Name the blood parasite species.
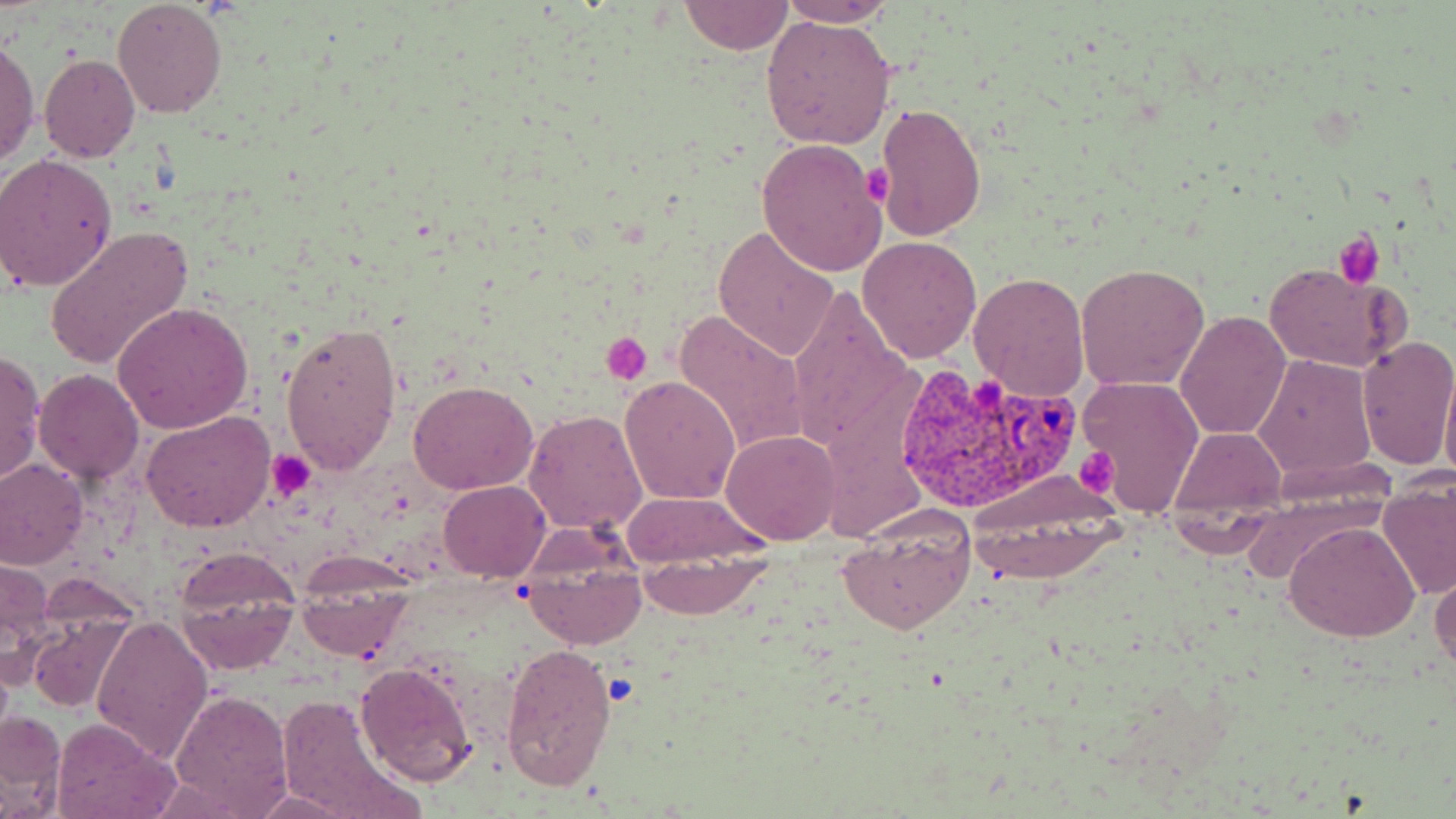

Plasmodium vivax.

{
  "image_size": "1456×819 pixels",
  "plasmodium_vivax_infected_red_blood_cell_locations": "approximate bounding boxes as [x1, y1, x2, y2] in pixels: [888, 361, 1081, 515]",
  "platelet_locations": "approximate bounding boxes as [x1, y1, x2, y2] in pixels: [864, 166, 894, 205], [1333, 230, 1385, 287], [600, 333, 652, 384], [1075, 446, 1121, 493], [269, 452, 315, 496]",
  "uninfected_red_blood_cell_locations": "approximate bounding boxes as [x1, y1, x2, y2] in pixels: [112, 1, 229, 119], [677, 1, 795, 55], [778, 1, 897, 27], [760, 16, 896, 149], [0, 37, 38, 171], [38, 54, 140, 163], [873, 102, 987, 240], [756, 139, 887, 276], [0, 153, 119, 292], [713, 225, 837, 363], [44, 226, 193, 371], [857, 236, 982, 364], [1262, 261, 1409, 373], [1075, 262, 1208, 392], [968, 270, 1090, 403], [786, 283, 914, 456], [112, 301, 254, 433], [673, 308, 807, 456], [1174, 311, 1292, 442], [280, 321, 403, 474], [1356, 335, 1456, 471], [0, 351, 46, 484], [1253, 353, 1379, 483], [1438, 362, 1456, 485], [32, 368, 144, 483], [1076, 375, 1205, 518], [619, 376, 742, 503], [408, 381, 539, 496], [525, 408, 650, 537], [141, 410, 274, 533], [1168, 426, 1286, 516], [721, 429, 840, 545], [0, 460, 86, 568], [438, 481, 550, 582], [620, 490, 770, 565], [1378, 490, 1456, 599], [961, 491, 1125, 586], [1164, 512, 1278, 557], [835, 516, 975, 636], [1284, 521, 1422, 643], [516, 528, 648, 651], [173, 547, 304, 674], [633, 552, 768, 617], [0, 554, 55, 680], [1430, 566, 1455, 679], [300, 574, 409, 660], [27, 613, 136, 715], [92, 615, 213, 763], [501, 641, 617, 791], [355, 662, 477, 787], [168, 687, 293, 819], [279, 695, 421, 818], [0, 709, 67, 815], [50, 719, 179, 819], [146, 775, 262, 816], [251, 791, 357, 818]",
  "modality": "light microscopy",
  "preparation": "thin blood film",
  "magnification": "1000x",
  "field_of_view": "single",
  "stain": "May-Grünwald-Giemsa"
}